Classify this cell by malaria status.
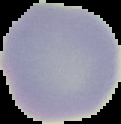
Uninfected.

image size = 121×124 pixels
image type = cell region segmented out of the field of view; surrounding area masked to black
preparation = thin blood film